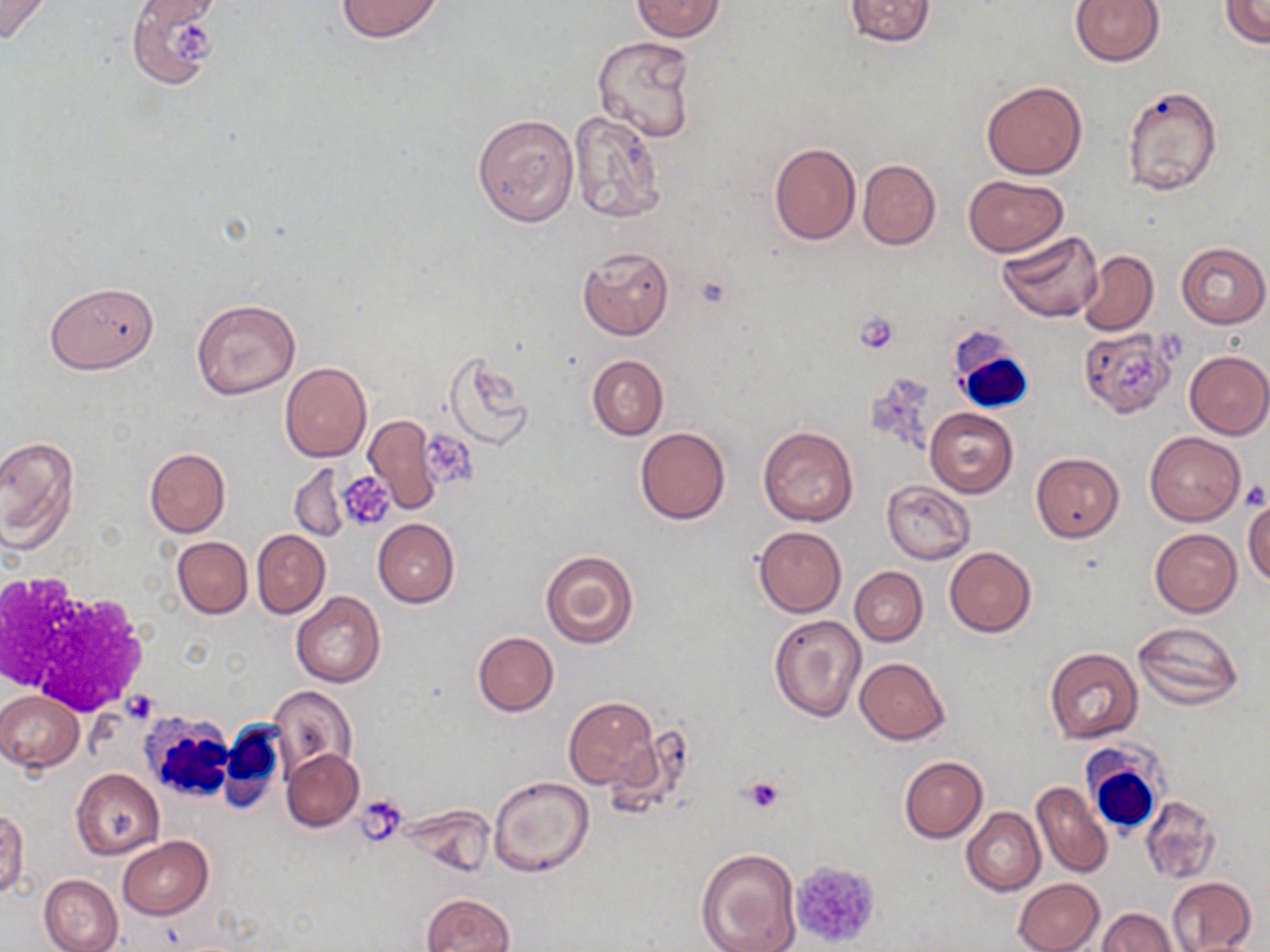
slide-level diagnosis = negative for blood parasites
image size = 1270×952 pixels
magnification = 1000x
stain = May-Grünwald-Giemsa
field of view = one of a larger specimen
modality = optical microscopy
preparation = thin blood smear
uninfected red blood cell locations = approximate bounding boxes as (x1, y1, x2, y2) in pixels: (0, 0, 52, 42), (334, 0, 445, 43), (631, 0, 725, 42), (844, 0, 936, 45), (1069, 0, 1165, 66), (1220, 0, 1270, 47), (137, 2, 220, 28), (126, 3, 223, 86), (591, 37, 698, 142), (982, 80, 1086, 180), (1122, 85, 1222, 196), (567, 111, 666, 224), (473, 112, 579, 227), (769, 142, 861, 246), (858, 159, 940, 250), (962, 175, 1069, 256), (971, 183, 1085, 316), (997, 232, 1103, 324), (1176, 242, 1269, 328), (577, 245, 676, 341), (1077, 249, 1158, 336), (45, 281, 159, 374), (192, 300, 301, 400), (1080, 330, 1176, 417), (1184, 350, 1270, 438), (443, 352, 531, 446), (587, 354, 668, 440), (280, 362, 371, 463), (925, 407, 1019, 497), (361, 413, 440, 513), (758, 426, 858, 525), (635, 427, 730, 524), (1146, 432, 1244, 526), (0, 435, 79, 553), (145, 447, 230, 538), (1030, 452, 1124, 542), (290, 465, 352, 542), (881, 481, 975, 564), (1243, 495, 1270, 587), (373, 519, 460, 607), (753, 526, 846, 618), (1151, 528, 1241, 617), (252, 530, 330, 619), (171, 536, 253, 619), (945, 547, 1035, 637), (539, 549, 640, 649), (849, 567, 927, 646), (291, 592, 385, 687), (768, 614, 869, 723), (1132, 622, 1244, 709), (472, 631, 559, 716), (1044, 648, 1142, 743), (855, 657, 949, 744), (269, 686, 358, 779), (0, 691, 84, 771), (564, 695, 659, 791), (281, 749, 362, 831), (898, 755, 987, 842), (72, 769, 164, 859), (488, 775, 595, 876), (1031, 782, 1112, 879), (1139, 795, 1221, 883), (0, 806, 29, 898), (962, 807, 1046, 897), (117, 837, 213, 919), (695, 847, 804, 952), (39, 874, 123, 952), (1167, 876, 1257, 952), (1013, 877, 1104, 952), (421, 893, 516, 952), (1099, 908, 1177, 952)
platelet locations = approximate bounding boxes as (x1, y1, x2, y2) in pixels: (170, 25, 216, 65), (855, 310, 898, 353), (1118, 354, 1156, 392), (425, 433, 477, 482), (337, 472, 395, 532), (1241, 479, 1269, 511), (122, 690, 159, 723), (744, 777, 785, 814), (355, 795, 407, 844), (787, 861, 880, 950)
white blood cell locations = approximate bounding boxes as (x1, y1, x2, y2) in pixels: (951, 336, 1037, 414), (3, 576, 150, 715), (140, 710, 229, 806), (220, 723, 286, 813), (1081, 743, 1168, 836)